Assess the morphology of the red blood cells.
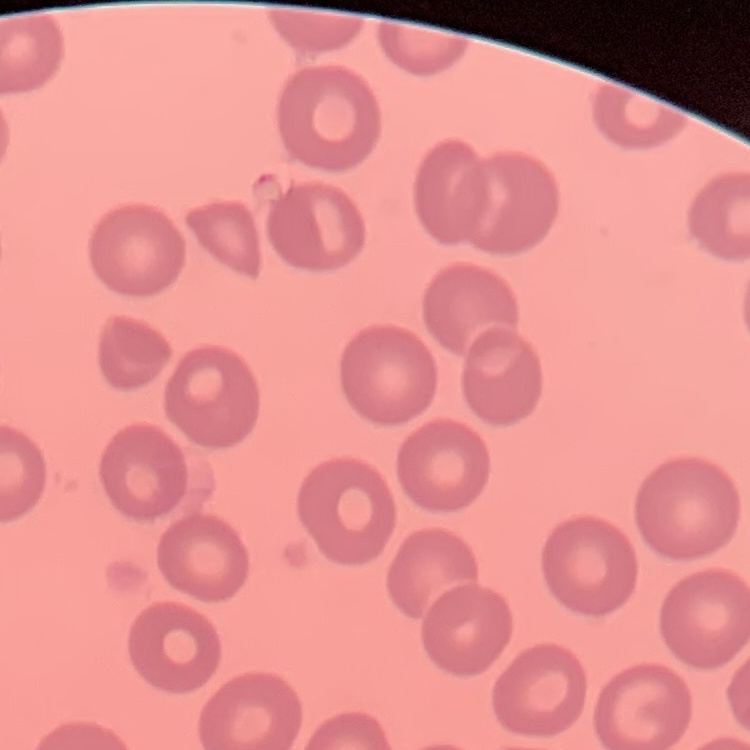
No rouleaux formation.

Summary:
  - Image type: square crop of a larger photomicrograph
  - Stain: Field's or Giemsa
  - Preparation: thin blood smear